Give the position of every Plasmodium parasite visible.
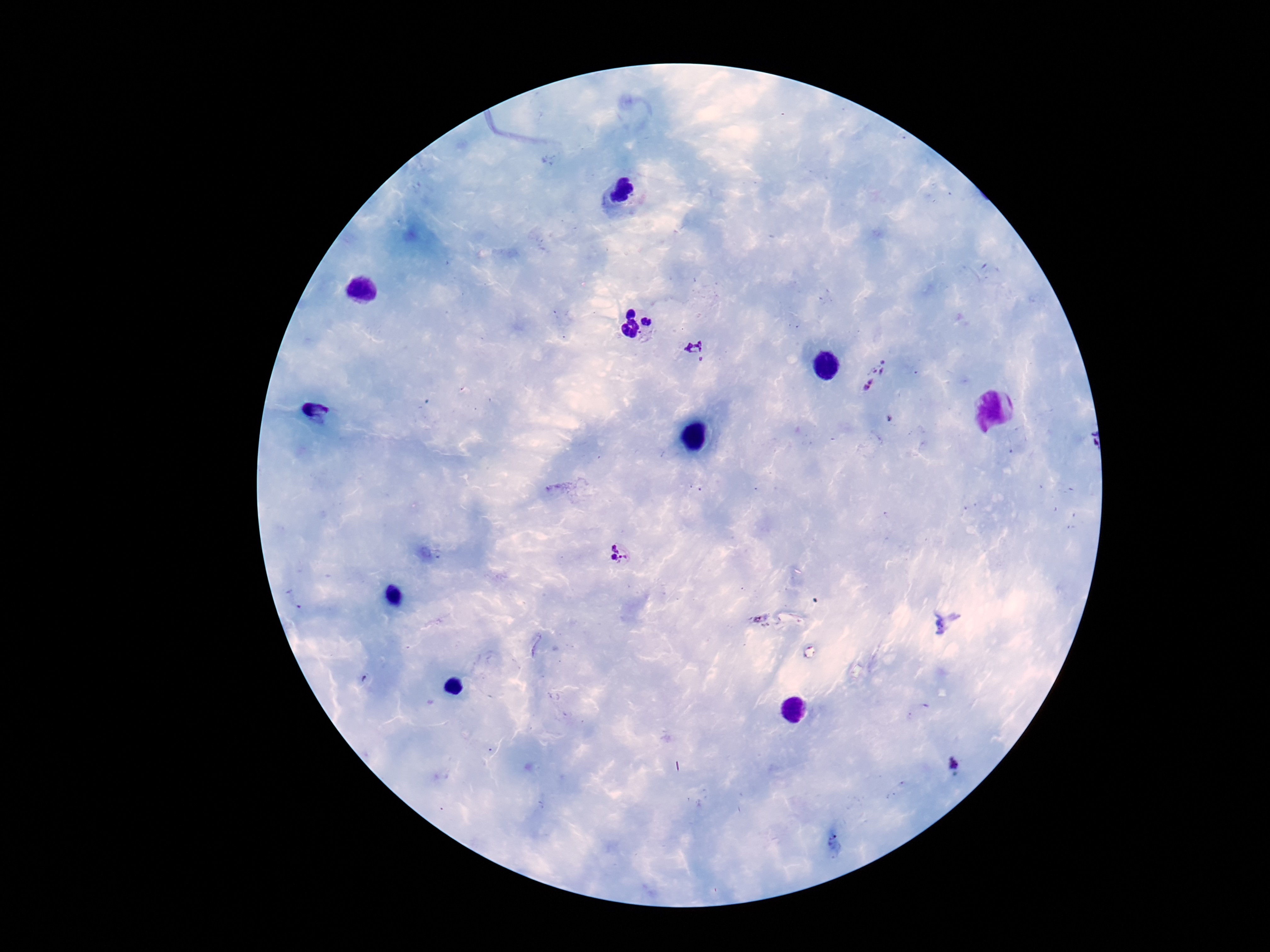
Approximate centers as {x, y} in pixels.
Plasmodium parasites: {696, 350}, {878, 376}, {620, 555}, {954, 766}.

Summary:
  - Patient malaria status: positive
  - Field of view: one from this slide
  - Preparation: thick peripheral-blood smear
  - Magnification: 100x
  - Capture: smartphone camera through the microscope eyepiece
  - Stain: Giemsa
  - Image size: 1270×952 pixels